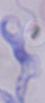
1000x magnification. A trypanosome is seen. Photomicrograph.